Identify the cell.
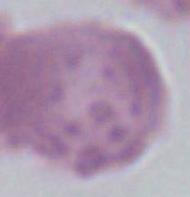
This is an erythrocyte.

Captured at 1000x magnification. Photomicrograph.